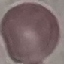
malaria status = uninfected
image type = cell patch, automatically extracted from a larger field of view and resized to 64 × 64 pixels
capture = smartphone camera at the microscope eyepiece
preparation = thin blood film
stain = Giemsa